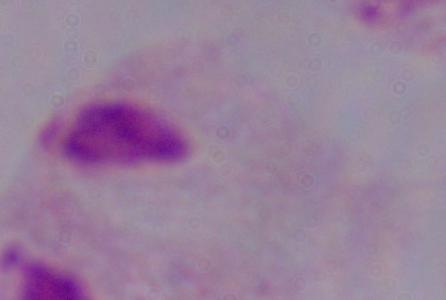
Summary:
  - Magnification: 1000x
  - Identification: trichomonad
  - Modality: photomicrograph